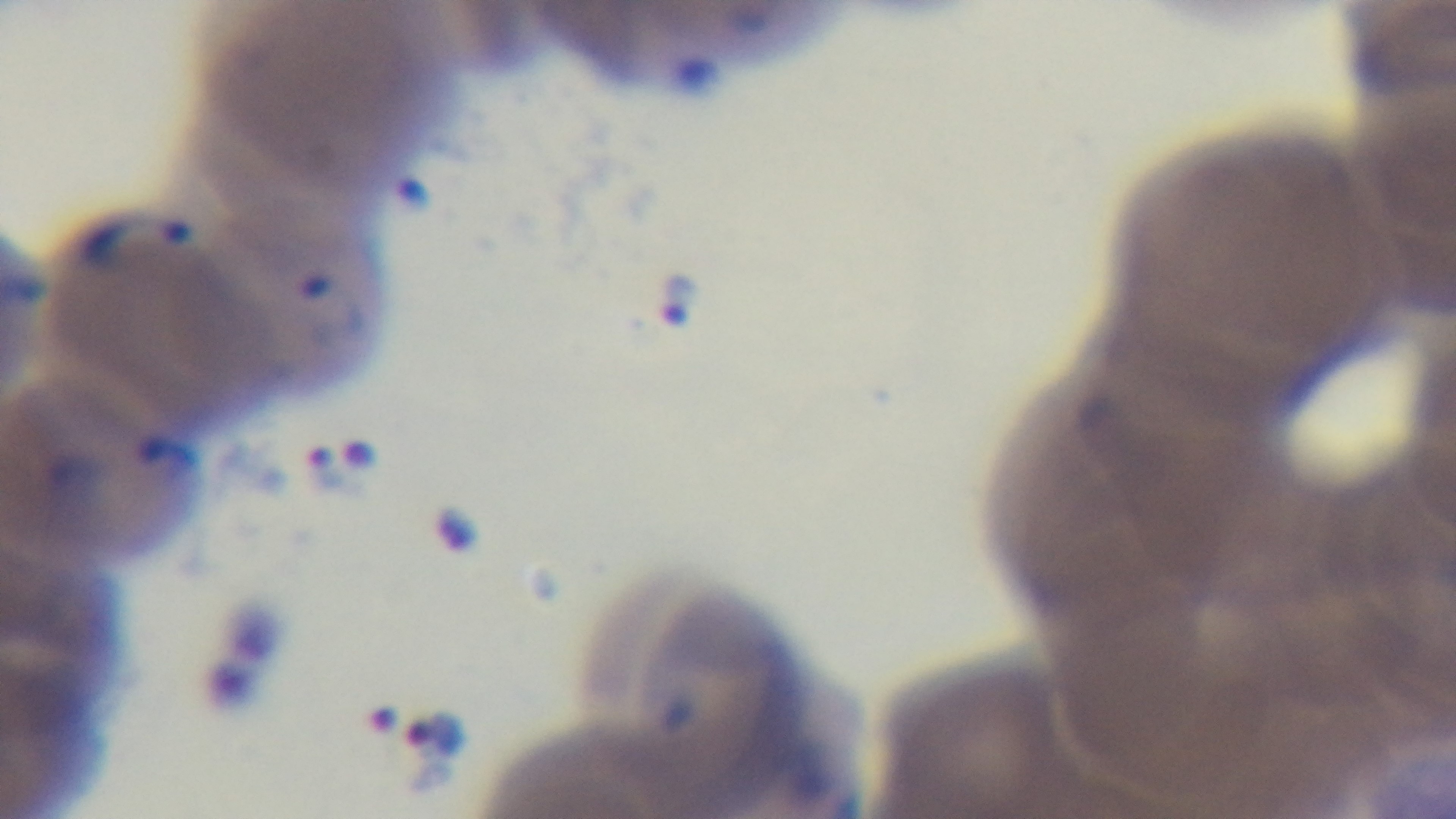
Giemsa-stained. Captured with a mounted 4K digital camera. 100x oil-immersion objective. Preparation: thin smear. Malaria status: positive. Photomicrograph. Single field of view.